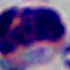

identification = white blood cell
magnification = 1000x
modality = micrograph